Identify the cell.
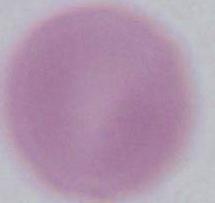
This is an erythrocyte.

Captured at 1000x magnification. Photomicrograph.